Report the malaria status of this cell.
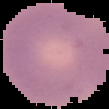

Uninfected.

From a thin blood film. The area outside the segmented cell region is set to black. Image is 109×109 pixels.